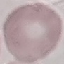

Malaria status: uninfected. Giemsa-stained preparation. Thin blood film. Acquired by smartphone through the microscope eyepiece. Cell patch, automatically extracted from a larger field of view and resized to 64 × 64 pixels.